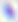
Summary:
  - Magnification: 400x
  - Identification: Toxoplasma gondii
  - Modality: photomicrograph